Identify the cell.
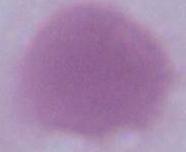
An erythrocyte.

magnification = 1000x
modality = photomicrograph